Assess this cell for malaria.
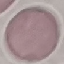

It is uninfected.

Summary:
  - Image type: cell patch, automatically extracted from a larger field of view and resized to 64 × 64 pixels
  - Preparation: thin blood film
  - Capture: smartphone camera at the microscope eyepiece
  - Stain: Giemsa